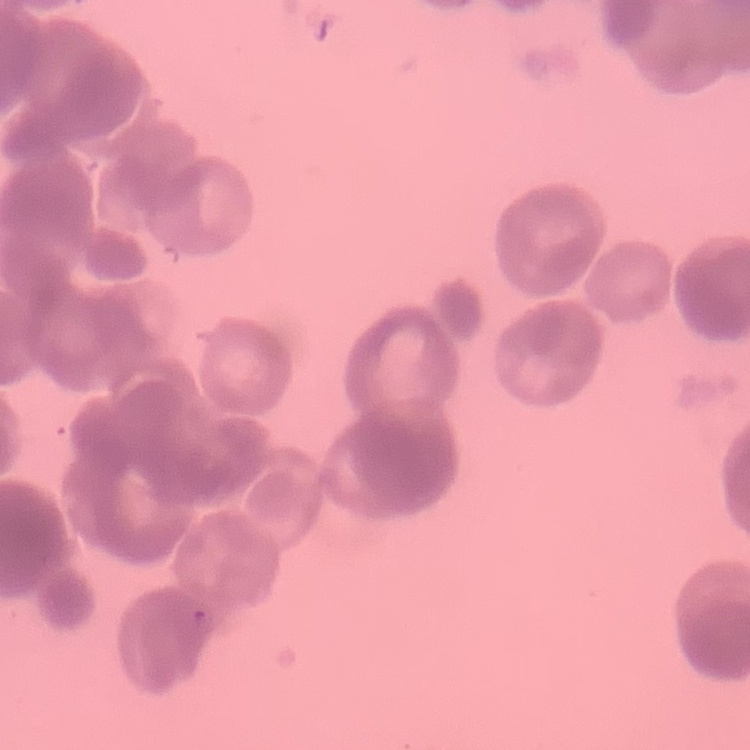

{
  "red_blood_cell_morphology": "rouleaux formation",
  "preparation": "thin peripheral smear",
  "image_type": "one tile cut from a larger photomicrograph",
  "stain": "Field's or Giemsa"
}